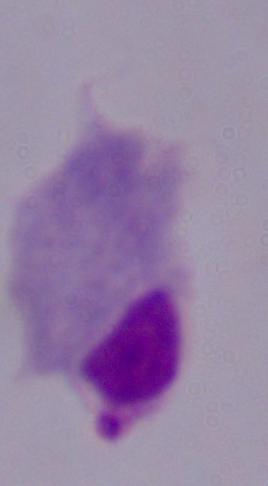
Summary:
  - Modality: photomicrograph
  - Identification: trichomonad
  - Magnification: 1000x